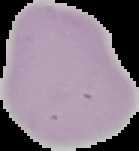

Malaria status: uninfected. Segmented cell region on a black background. From a thin blood film. Image is 139×151 pixels.